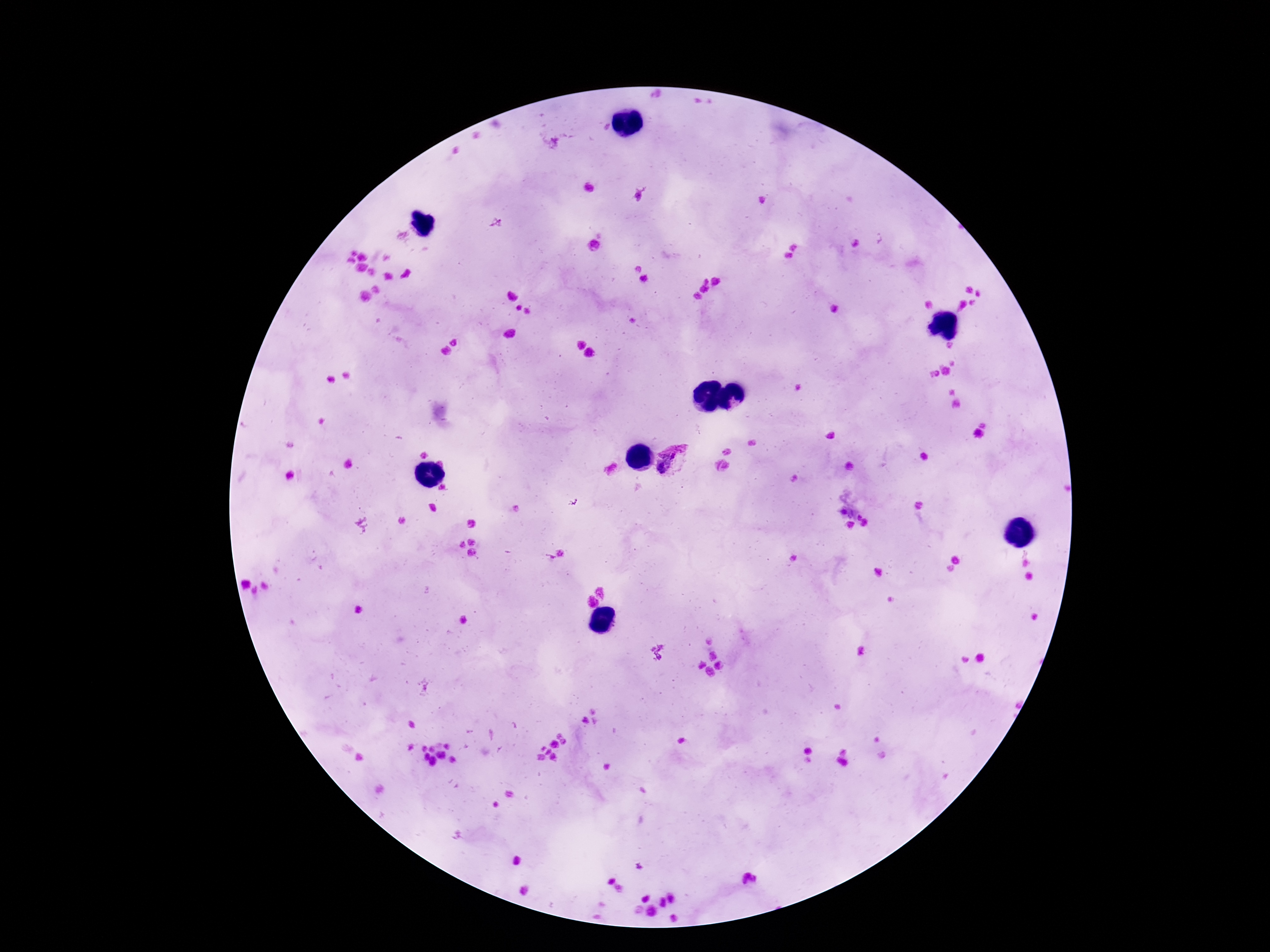
Approximate centers as {x, y} in pixels.
Summary:
  - Plasmodium parasite locations: {673, 462}
  - Field of view: single
  - Capture: smartphone camera through the microscope eyepiece
  - Stain: Giemsa
  - Magnification: 100x
  - Preparation: thick peripheral-blood smear
  - Patient malaria status: positive
  - Image size: 1270×952 pixels